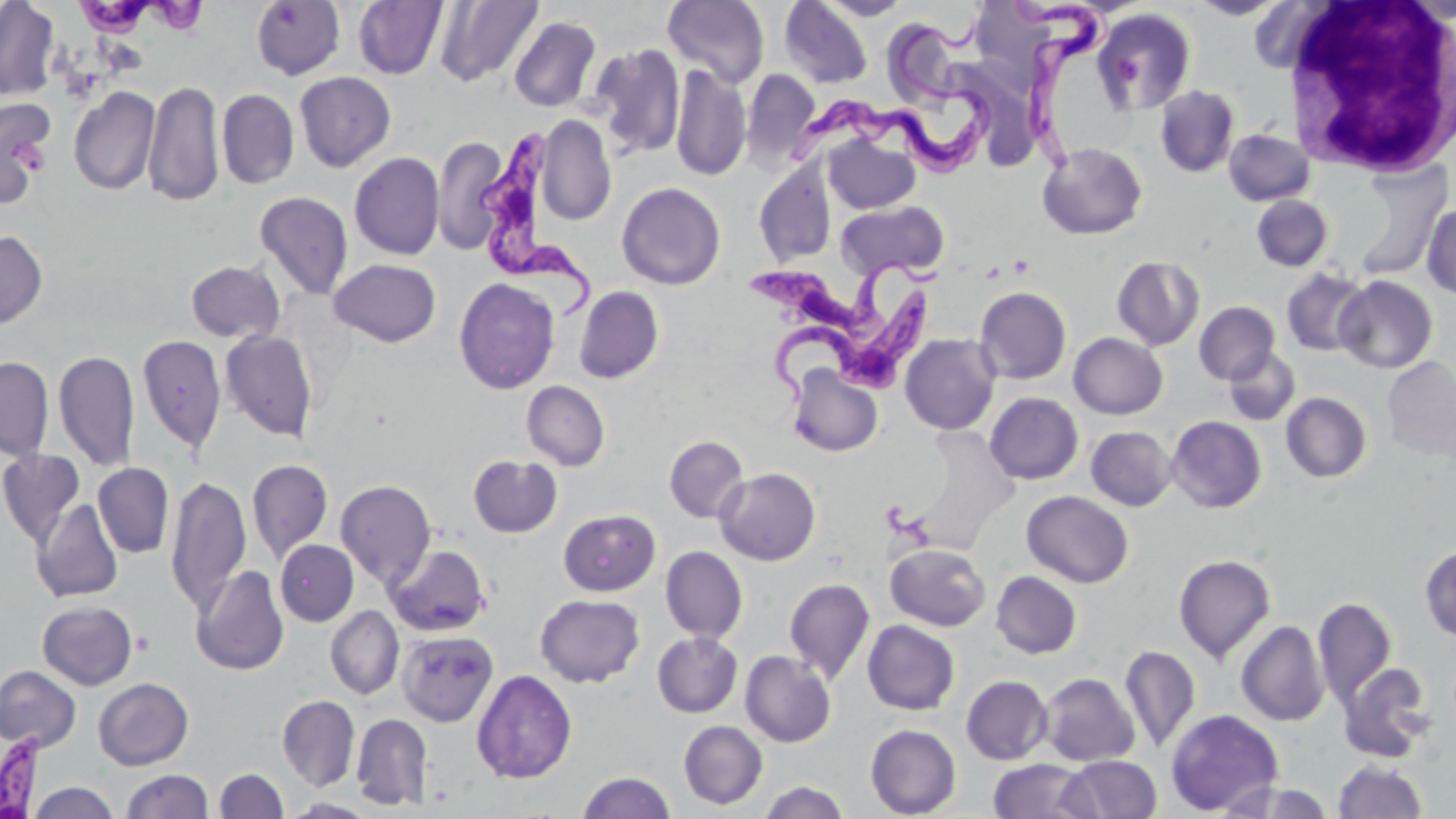

Approximate bounding boxes as (x1,y1)-(x2,y2) corner pairs in pixels. Trypanosoma brucei locations: (75,0)-(209,42), (1001,0)-(1115,180), (783,15)-(993,179), (477,125)-(599,324), (744,251)-(952,347), (774,289)-(932,403). Uninfected red blood cell locations: (0,0)-(59,101), (435,0)-(543,86), (780,0)-(873,89), (818,0)-(911,20), (977,0)-(1056,94), (1189,0)-(1288,20), (251,1)-(345,79), (353,1)-(448,80), (662,1)-(769,88), (1093,8)-(1196,115), (509,16)-(601,112), (887,23)-(959,115), (590,44)-(685,158), (950,59)-(1042,174), (670,64)-(751,182), (741,70)-(820,167), (294,72)-(396,172), (143,79)-(224,208), (68,86)-(161,196), (1155,86)-(1239,178), (217,89)-(299,189), (0,100)-(54,205), (537,114)-(616,225), (1223,129)-(1314,206), (433,134)-(508,255), (823,135)-(920,214), (1037,142)-(1148,240), (349,152)-(445,260), (1342,160)-(1451,281), (753,161)-(837,267), (616,182)-(726,290), (254,191)-(353,301), (1250,195)-(1333,272), (837,200)-(949,281), (1421,202)-(1456,299), (0,230)-(47,328), (1112,256)-(1204,350), (329,259)-(441,347), (186,260)-(285,343), (1282,268)-(1371,356), (1335,276)-(1437,373), (454,277)-(560,394), (574,286)-(664,384), (975,286)-(1071,384), (1194,301)-(1280,384), (220,330)-(318,441), (1069,332)-(1167,419), (137,334)-(227,454), (900,334)-(1000,435), (1223,348)-(1301,426), (54,349)-(139,471), (0,356)-(54,459), (1383,359)-(1455,458), (787,365)-(883,457), (521,381)-(610,471), (985,392)-(1083,484), (1280,392)-(1371,483), (1167,416)-(1266,513), (1086,426)-(1176,511), (664,436)-(748,522), (0,449)-(86,547), (467,455)-(562,538), (247,459)-(333,562), (93,463)-(174,558), (715,467)-(821,565), (166,474)-(251,615), (335,480)-(436,587), (1022,491)-(1134,588), (32,498)-(124,602), (558,509)-(660,596), (555,510)-(652,688), (275,540)-(358,626), (383,543)-(491,636), (885,543)-(991,631), (1419,545)-(1456,641), (660,546)-(748,643), (1173,554)-(1276,664), (192,565)-(289,676), (991,571)-(1081,659), (784,577)-(875,684), (534,593)-(644,687), (1313,596)-(1397,709), (37,600)-(137,690), (325,606)-(404,699), (863,620)-(960,715), (1236,621)-(1328,726), (397,630)-(499,727), (653,632)-(742,718), (1119,645)-(1200,754), (740,650)-(836,747), (1338,661)-(1436,763), (0,665)-(81,752), (472,669)-(577,783), (1039,673)-(1139,766), (961,675)-(1052,765), (93,677)-(193,770), (277,695)-(360,791), (1165,709)-(1284,815), (351,713)-(433,810), (678,721)-(767,809), (865,724)-(961,818), (1060,756)-(1161,819), (987,759)-(1094,819), (1331,759)-(1428,818), (215,768)-(288,819), (122,769)-(213,819), (578,771)-(676,818), (758,781)-(850,819), (1221,781)-(1335,819), (27,782)-(120,818), (284,798)-(379,818). White blood cell locations: (1283,0)-(1456,176). Platelet locations: (1115,57)-(1143,85). Slide-level diagnosis: Trypanosoma brucei. Thin blood smear. May-Grünwald-Giemsa-stained preparation. 1000x magnification. One field of a larger specimen. Light microscopy. Image is 1456×819 pixels.